Classify this cell by malaria status.
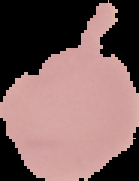
Uninfected.

Summary:
  - Preparation: thin blood film
  - Image size: 139×181 pixels
  - Image type: segmented cell region with the area outside set to black